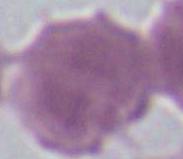
modality: photomicrograph
identification: red blood cell
magnification: 1000x